Give the position of every Plasmodium falciparum parasite, noting its life-cycle stage.
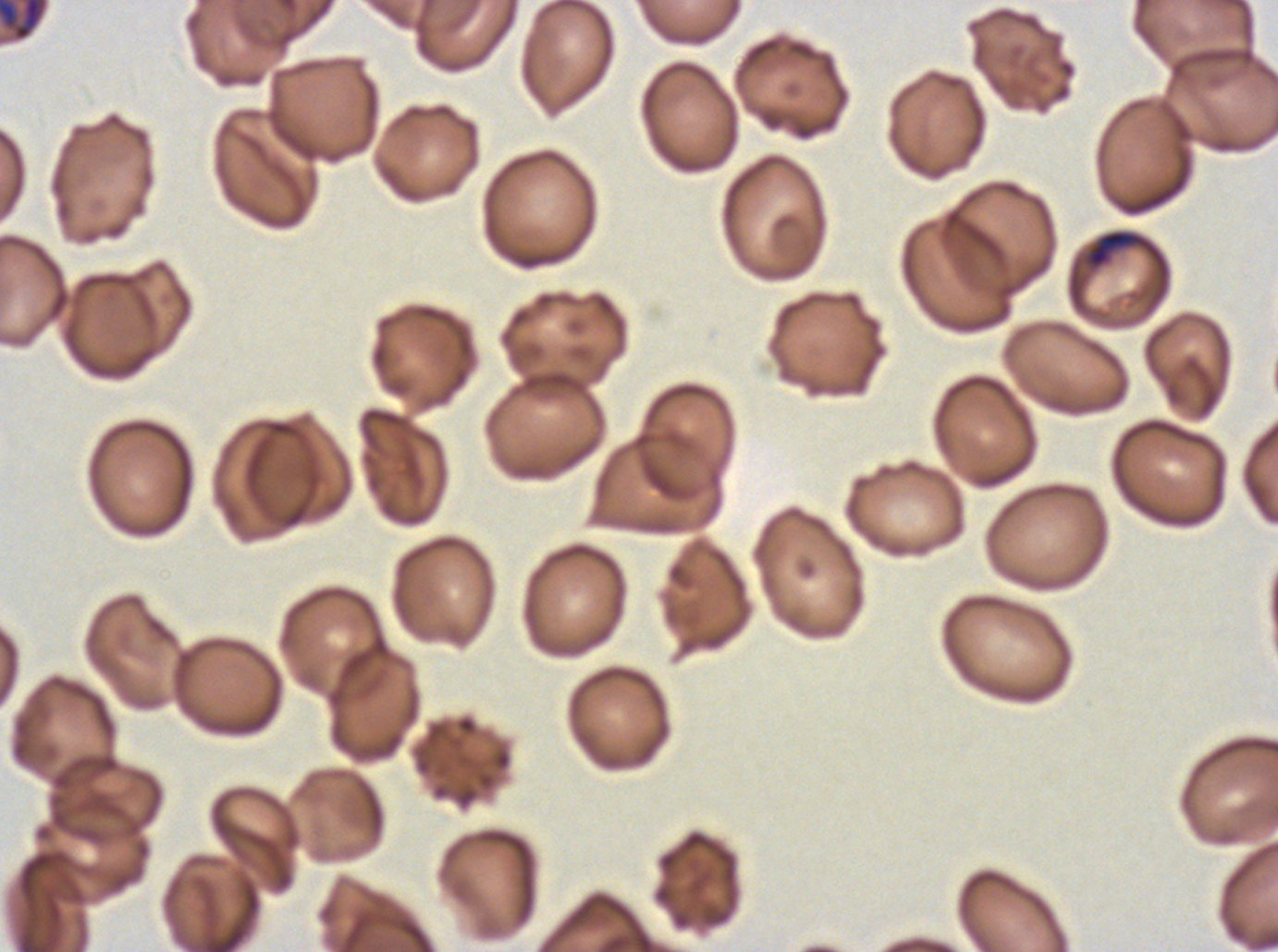
Approximate bounding boxes as (x1, y1, x2, y2) in pixels.
Late-ring/early-trophozoite forms: (1087, 230, 1140, 268).
Mid trophozoites: (0, 0, 49, 43).
No rings, late trophozoites, early schizonts, late schizonts, segmenters, or gametocytes observed.

{
  "specimen": "Plasmodium falciparum from a patient in The Gambia, cultured ex vivo for 24 to 48 hours",
  "stain": "Giemsa",
  "life_cycle_stages_observed": "late-ring/early-trophozoite, mid trophozoite",
  "image_size": "1278×952 pixels",
  "preparation": "thin blood film",
  "field_of_view": "sub-image separated from a larger composite"
}